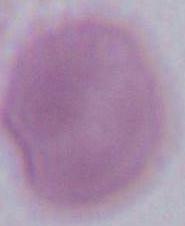
Summary:
  - Magnification: 1000x
  - Identification: erythrocyte
  - Modality: micrograph